State the blood parasite species.
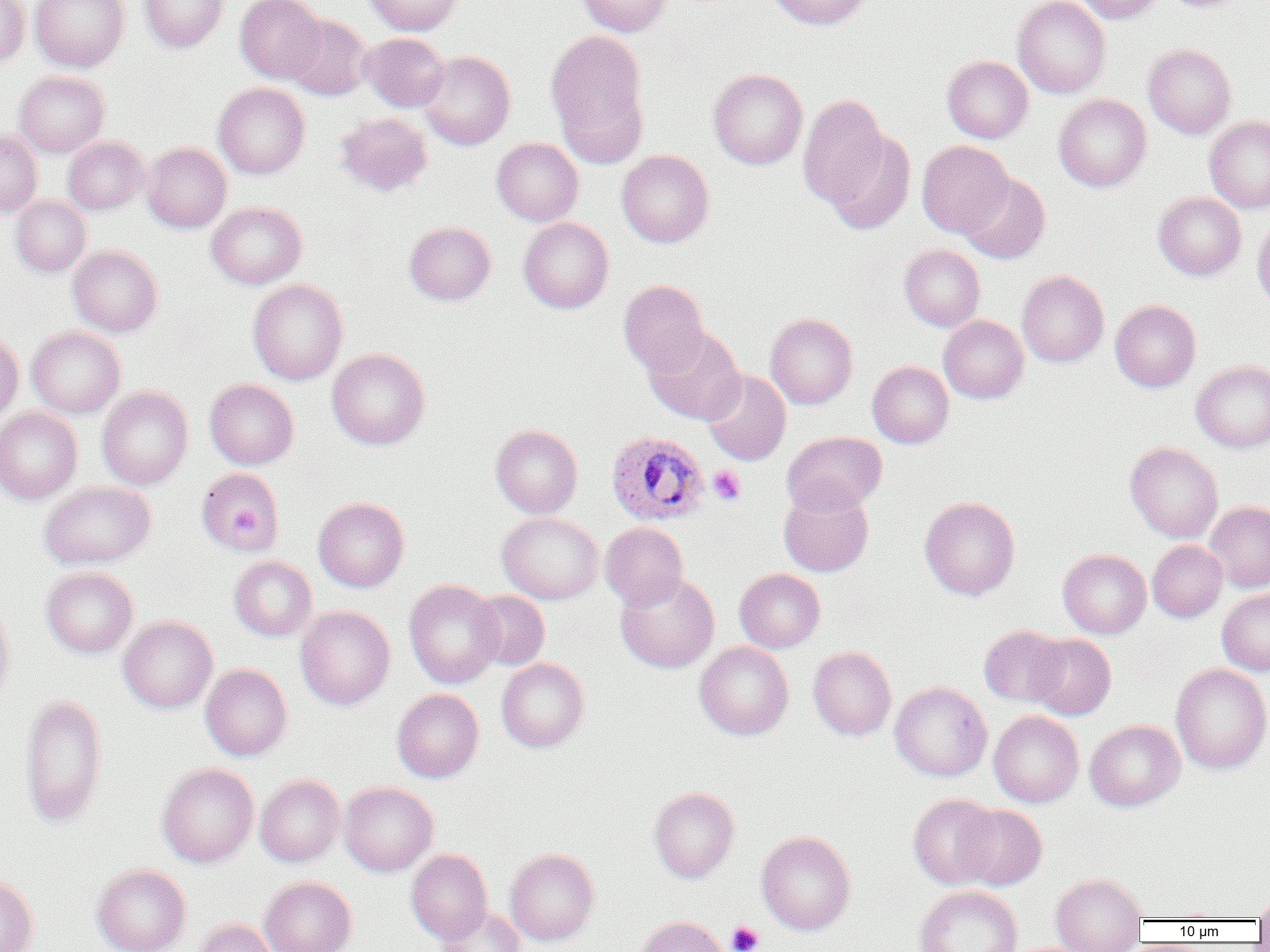

Plasmodium ovale.

Summary:
  - Coordinate format: approximate bounding boxes as [x1, y1, x2, y2] in pixels
  - Platelet locations: [708, 465, 746, 505], [231, 504, 261, 536], [727, 920, 764, 952]
  - Plasmodium ovale-infected red blood cell locations: [605, 430, 710, 526]
  - Uninfected red blood cell locations: [0, 0, 30, 67], [30, 0, 130, 72], [140, 0, 228, 53], [235, 0, 326, 84], [363, 0, 463, 36], [576, 0, 672, 37], [767, 0, 872, 29], [1012, 0, 1110, 98], [1073, 0, 1164, 24], [1160, 0, 1249, 13], [284, 14, 372, 101], [545, 29, 648, 153], [359, 32, 449, 112], [1143, 43, 1236, 138], [417, 50, 516, 150], [942, 56, 1033, 143], [708, 68, 807, 170], [14, 71, 109, 157], [213, 83, 310, 179], [797, 94, 889, 209], [1053, 94, 1151, 192], [334, 112, 433, 197], [1204, 116, 1270, 214], [0, 130, 42, 217], [822, 130, 916, 234], [63, 136, 149, 214], [491, 137, 583, 226], [917, 140, 1013, 237], [142, 143, 231, 232], [616, 149, 714, 248], [958, 173, 1050, 264], [1153, 192, 1246, 280], [10, 196, 91, 277], [206, 202, 307, 289], [1252, 214, 1270, 313], [518, 217, 614, 314], [404, 221, 496, 305], [899, 245, 985, 332], [68, 246, 163, 337], [1016, 270, 1109, 368], [247, 279, 348, 385], [618, 279, 709, 375], [1110, 300, 1201, 392], [765, 313, 858, 409], [939, 315, 1029, 404], [26, 326, 125, 418], [643, 326, 746, 425], [0, 332, 23, 423], [327, 348, 430, 450], [1190, 360, 1270, 453], [867, 361, 954, 448], [702, 370, 791, 465], [205, 379, 298, 469], [97, 386, 193, 489], [0, 407, 82, 504], [490, 424, 583, 518], [781, 431, 887, 516], [1125, 442, 1223, 543], [196, 468, 283, 554], [39, 481, 156, 569], [778, 487, 874, 577], [919, 496, 1020, 601], [313, 497, 409, 592], [1204, 501, 1270, 593], [497, 512, 603, 604], [600, 522, 688, 611], [1147, 540, 1227, 622], [1058, 549, 1151, 638], [228, 556, 317, 641], [41, 567, 138, 658], [734, 568, 825, 653], [615, 571, 719, 673], [403, 579, 504, 689], [1218, 589, 1270, 676], [468, 590, 550, 670], [0, 598, 15, 710], [295, 605, 395, 710], [118, 616, 217, 713], [979, 625, 1069, 707], [1028, 634, 1115, 720], [694, 641, 794, 741], [808, 646, 896, 740], [496, 658, 590, 753], [200, 663, 292, 761], [1170, 663, 1270, 774], [890, 681, 992, 782], [392, 689, 484, 783], [19, 694, 107, 830], [989, 710, 1084, 807], [1085, 720, 1185, 811], [156, 763, 259, 868], [255, 774, 345, 867], [339, 782, 438, 876], [648, 786, 739, 883], [907, 794, 1001, 889], [955, 804, 1047, 890], [756, 830, 855, 935], [504, 848, 599, 945], [406, 849, 492, 943], [91, 863, 191, 952], [0, 872, 39, 952], [1051, 873, 1148, 952], [259, 876, 357, 952], [914, 885, 1022, 952], [1253, 892, 1270, 924], [436, 906, 526, 952], [634, 915, 729, 952], [192, 919, 279, 952]
  - Image size: 1270×952 pixels
  - Magnification: 1000x
  - Field of view: single
  - Preparation: thin blood smear
  - Modality: light microscopy